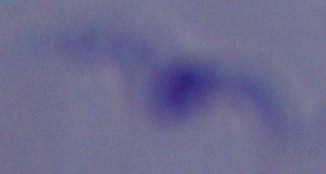

identification: trypanosome
modality: micrograph
magnification: 1000x